Identify the parasite.
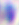

Toxoplasma gondii.

Summary:
  - Magnification: 400x
  - Modality: photomicrograph